Give the extent of all Plasmodium ovale-infected red blood cells.
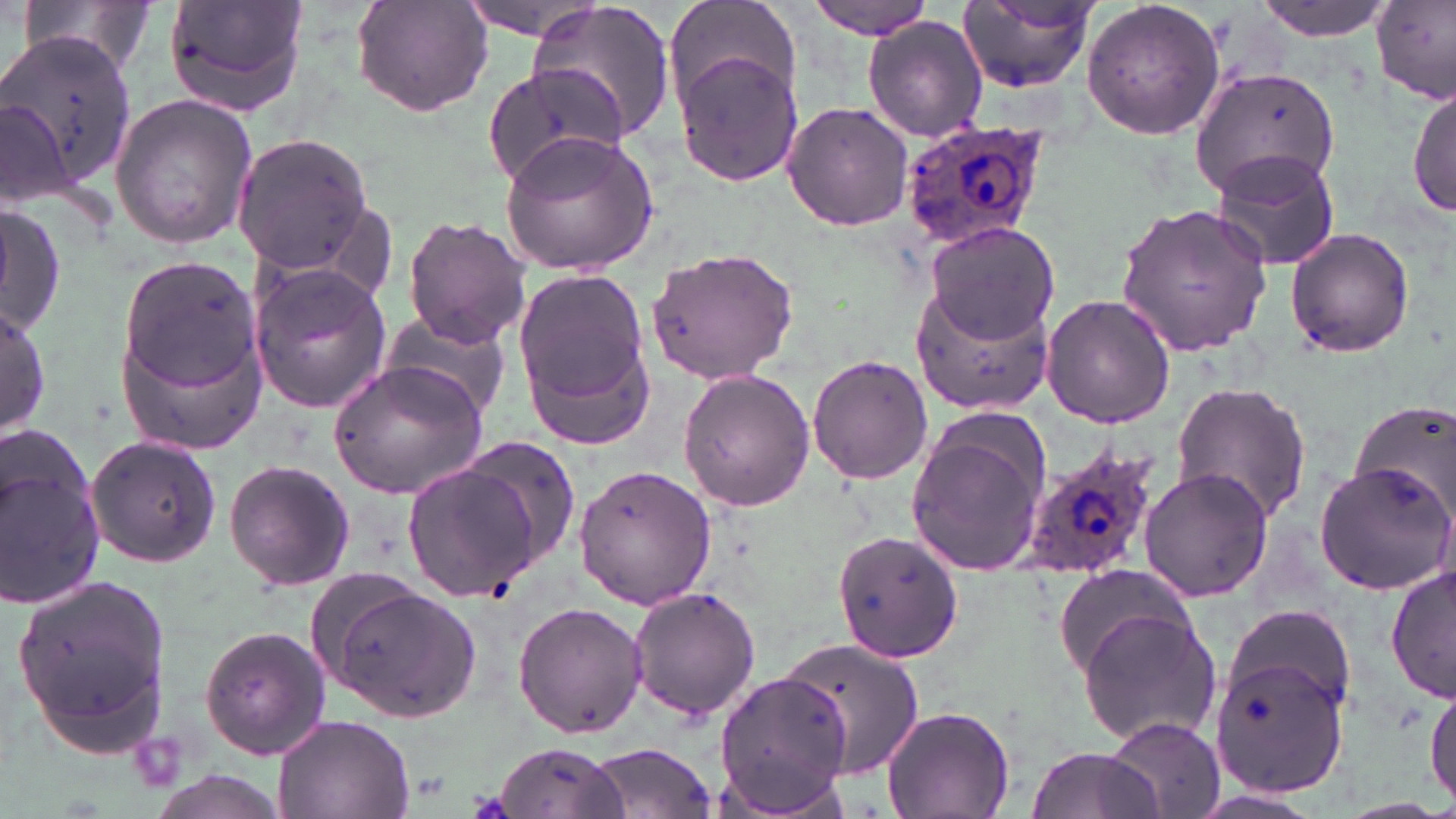
Approximate bounding boxes as [x1, y1, x2, y2] in pixels.
Plasmodium ovale-infected red blood cells: [897, 118, 1053, 251], [1018, 440, 1166, 587].

Summary:
  - Uninfected red blood cell locations: [21, 0, 159, 80], [163, 0, 308, 115], [457, 0, 609, 39], [526, 0, 676, 147], [803, 0, 936, 37], [1081, 0, 1226, 141], [1253, 0, 1399, 41], [351, 1, 493, 117], [956, 1, 1096, 92], [664, 2, 805, 116], [1373, 2, 1456, 103], [862, 15, 988, 141], [1, 41, 124, 198], [674, 51, 803, 188], [481, 63, 626, 190], [1190, 65, 1340, 196], [1410, 83, 1455, 220], [108, 92, 259, 251], [0, 93, 73, 207], [781, 101, 914, 231], [500, 130, 660, 276], [232, 133, 374, 272], [1210, 150, 1345, 274], [1116, 201, 1274, 356], [1, 203, 64, 336], [309, 203, 399, 301], [403, 216, 532, 347], [923, 220, 1062, 349], [1284, 227, 1415, 360], [644, 245, 800, 385], [116, 253, 262, 405], [248, 263, 390, 414], [515, 269, 655, 425], [911, 280, 1056, 416], [1042, 293, 1176, 429], [0, 297, 50, 439], [112, 309, 271, 455], [380, 312, 511, 421], [530, 335, 650, 452], [807, 354, 933, 485], [328, 361, 488, 501], [677, 368, 816, 513], [1169, 380, 1314, 524], [1349, 397, 1456, 526], [907, 430, 1049, 572], [85, 435, 222, 568], [456, 436, 583, 565], [0, 449, 105, 614], [225, 459, 354, 591], [405, 459, 545, 600], [1313, 462, 1453, 596], [574, 463, 715, 610], [1137, 466, 1275, 603], [832, 526, 962, 662], [1056, 561, 1196, 676], [1386, 562, 1456, 706], [12, 570, 173, 753], [316, 577, 480, 721], [630, 586, 762, 723], [513, 601, 647, 738], [1226, 603, 1353, 715], [1075, 606, 1222, 749], [199, 624, 330, 761], [774, 637, 927, 776], [1209, 655, 1349, 796], [711, 670, 854, 816], [1427, 680, 1456, 809], [881, 705, 1015, 817], [274, 711, 414, 819], [1103, 717, 1225, 819], [493, 740, 628, 819], [584, 741, 718, 817], [1026, 745, 1174, 819]
  - Slide-level diagnosis: Plasmodium ovale
  - Magnification: 1000x
  - Image size: 1456×819 pixels
  - Stain: May-Grünwald-Giemsa
  - Preparation: thin blood smear
  - Field of view: one of a larger specimen
  - Modality: optical microscopy